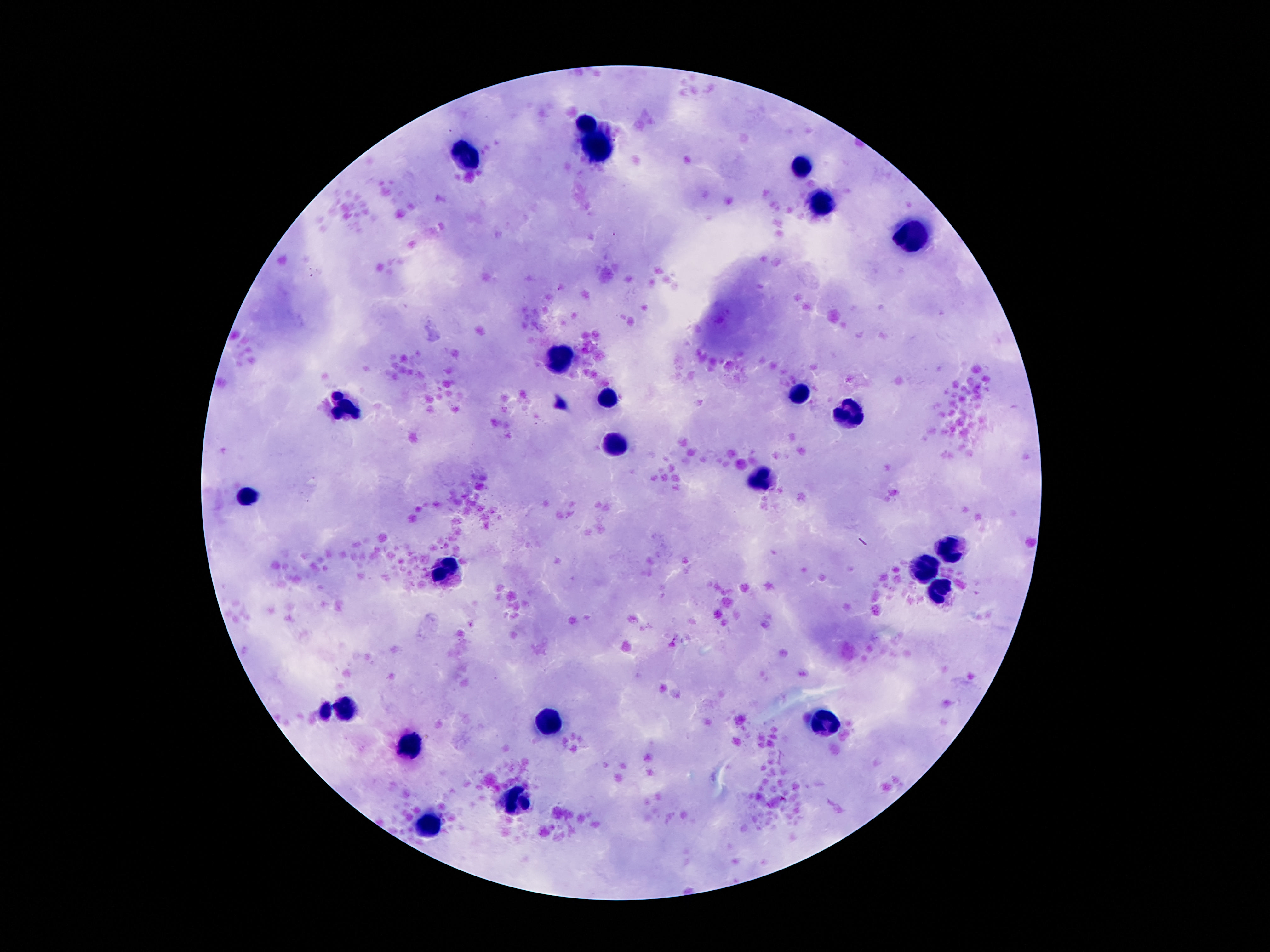
Approximate centers as (x, y) in pixels.
Summary:
  - Leukocyte locations: (587, 123), (604, 155), (469, 157), (799, 165), (822, 204), (915, 238), (564, 360), (797, 396), (606, 398), (345, 407), (849, 411), (618, 447), (759, 480), (251, 493), (950, 545), (446, 566), (925, 570), (933, 596), (349, 707), (327, 714), (822, 721), (551, 723), (412, 745), (515, 799), (429, 826)
  - Preparation: thick peripheral-blood smear
  - Stain: Giemsa
  - Patient malaria status: not infected
  - Capture: smartphone camera through the microscope eyepiece
  - Image size: 1270×952 pixels
  - Field of view: single
  - Magnification: 100x